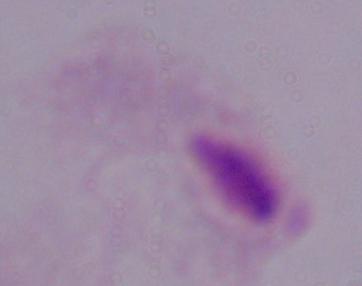 A trichomonad is seen. Photomicrograph. Captured at 1000x magnification.